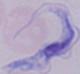
A trypanosome is shown. Micrograph. Captured at 1000x magnification.